Report the malaria status of this cell.
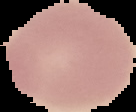
Uninfected.

Summary:
  - Image type: cell region segmented out of the field of view; surrounding area masked to black
  - Preparation: thin blood film
  - Image size: 136×112 pixels